Locate and identify every blood parasite.
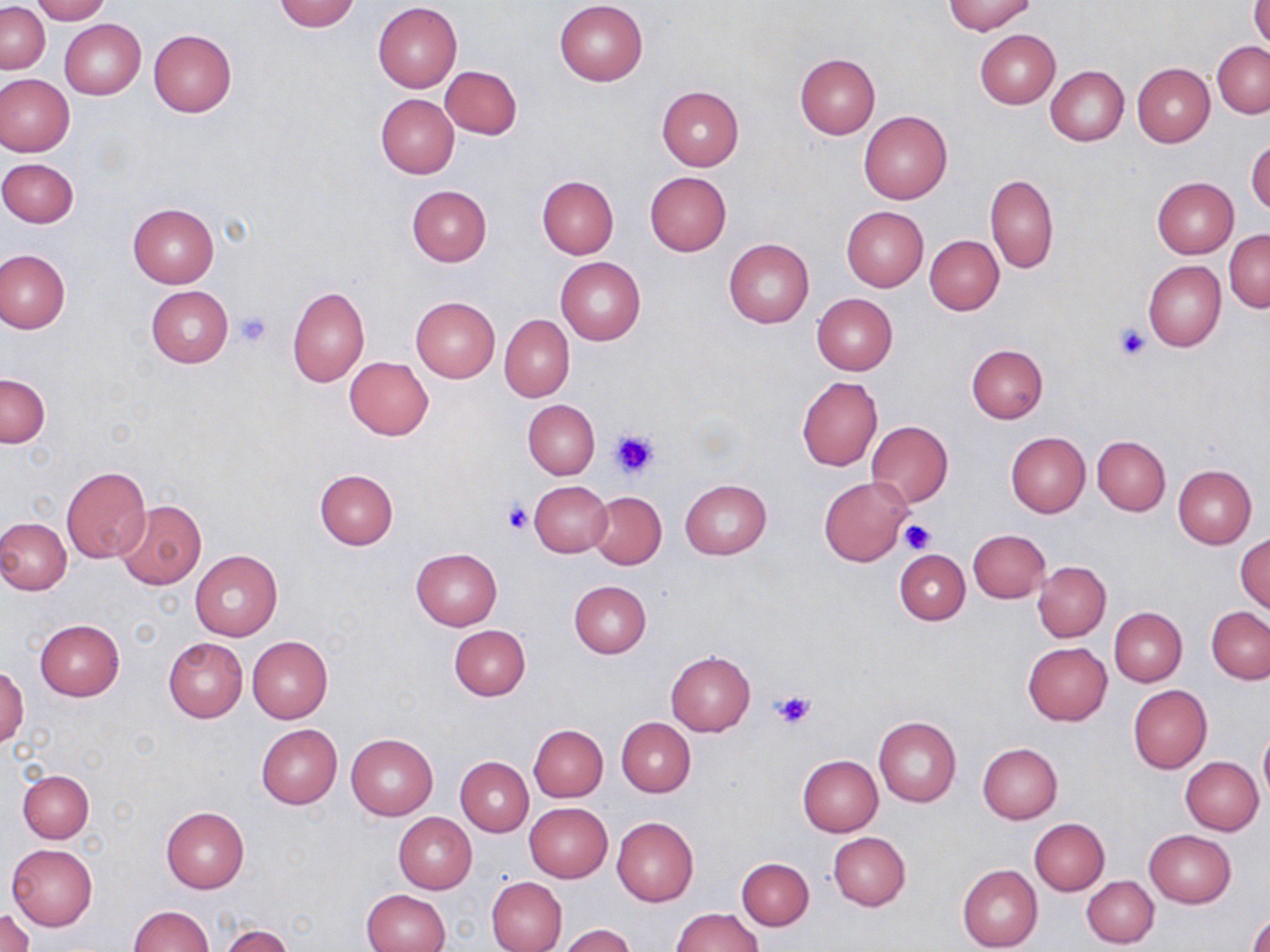

No blood parasites seen.

slide-level diagnosis = no evidence of blood parasites
platelet locations = approximate bounding boxes as named x1/y1/x2/y2 corners in pixels: (x1=231, y1=309, x2=273, y2=346), (x1=1114, y1=324, x2=1150, y2=361), (x1=608, y1=427, x2=662, y2=480), (x1=503, y1=501, x2=534, y2=535), (x1=900, y1=519, x2=936, y2=554), (x1=771, y1=689, x2=816, y2=729)
modality = light microscopy
stain = May-Grünwald-Giemsa
image size = 1270×952 pixels
uninfected red blood cell locations = approximate bounding boxes as named x1/y1/x2/y2 corners in pixels: (x1=30, y1=0, x2=109, y2=23), (x1=274, y1=0, x2=361, y2=32), (x1=943, y1=0, x2=1035, y2=34), (x1=373, y1=1, x2=462, y2=91), (x1=554, y1=1, x2=647, y2=85), (x1=1250, y1=1, x2=1270, y2=51), (x1=1, y1=3, x2=49, y2=73), (x1=59, y1=19, x2=144, y2=99), (x1=975, y1=29, x2=1060, y2=108), (x1=149, y1=30, x2=237, y2=117), (x1=1213, y1=41, x2=1270, y2=117), (x1=794, y1=53, x2=880, y2=138), (x1=1131, y1=63, x2=1214, y2=147), (x1=440, y1=65, x2=521, y2=139), (x1=1045, y1=65, x2=1129, y2=145), (x1=0, y1=75, x2=74, y2=156), (x1=656, y1=86, x2=743, y2=171), (x1=375, y1=93, x2=459, y2=178), (x1=859, y1=110, x2=953, y2=204), (x1=1247, y1=138, x2=1270, y2=214), (x1=0, y1=157, x2=78, y2=227), (x1=644, y1=171, x2=731, y2=256), (x1=985, y1=174, x2=1058, y2=275), (x1=536, y1=176, x2=618, y2=258), (x1=1152, y1=177, x2=1238, y2=258), (x1=406, y1=185, x2=491, y2=267), (x1=127, y1=204, x2=219, y2=288), (x1=841, y1=206, x2=929, y2=291), (x1=1225, y1=230, x2=1269, y2=312), (x1=925, y1=235, x2=1003, y2=315), (x1=723, y1=239, x2=813, y2=328), (x1=0, y1=249, x2=69, y2=332), (x1=555, y1=257, x2=645, y2=344), (x1=1144, y1=260, x2=1226, y2=352), (x1=146, y1=286, x2=233, y2=368), (x1=288, y1=287, x2=369, y2=386), (x1=813, y1=294, x2=897, y2=374), (x1=411, y1=296, x2=500, y2=381), (x1=499, y1=314, x2=574, y2=402), (x1=966, y1=344, x2=1048, y2=423), (x1=344, y1=357, x2=433, y2=440), (x1=1, y1=373, x2=50, y2=447), (x1=796, y1=376, x2=882, y2=471), (x1=523, y1=400, x2=600, y2=479), (x1=866, y1=420, x2=952, y2=508), (x1=1005, y1=431, x2=1090, y2=517), (x1=1093, y1=436, x2=1171, y2=515), (x1=61, y1=465, x2=151, y2=563), (x1=1173, y1=465, x2=1256, y2=548), (x1=314, y1=468, x2=398, y2=550), (x1=819, y1=476, x2=911, y2=565), (x1=680, y1=479, x2=771, y2=559), (x1=529, y1=481, x2=612, y2=558), (x1=589, y1=491, x2=667, y2=568), (x1=116, y1=500, x2=206, y2=590), (x1=0, y1=518, x2=71, y2=596), (x1=968, y1=529, x2=1051, y2=603), (x1=1236, y1=533, x2=1270, y2=614), (x1=411, y1=548, x2=502, y2=631), (x1=894, y1=548, x2=969, y2=624), (x1=190, y1=551, x2=282, y2=640), (x1=1033, y1=561, x2=1111, y2=641), (x1=568, y1=580, x2=651, y2=658), (x1=1109, y1=607, x2=1187, y2=686), (x1=1207, y1=607, x2=1270, y2=683), (x1=34, y1=620, x2=125, y2=701), (x1=448, y1=624, x2=530, y2=700), (x1=247, y1=635, x2=333, y2=722), (x1=163, y1=637, x2=249, y2=722), (x1=1023, y1=642, x2=1112, y2=725), (x1=665, y1=651, x2=755, y2=736), (x1=1, y1=667, x2=28, y2=748), (x1=1129, y1=686, x2=1212, y2=773), (x1=873, y1=716, x2=961, y2=806), (x1=615, y1=717, x2=695, y2=797), (x1=256, y1=723, x2=342, y2=808), (x1=528, y1=725, x2=607, y2=802), (x1=1259, y1=727, x2=1270, y2=804), (x1=346, y1=733, x2=438, y2=820), (x1=976, y1=743, x2=1062, y2=823), (x1=797, y1=754, x2=883, y2=836), (x1=1181, y1=756, x2=1265, y2=835), (x1=456, y1=757, x2=533, y2=835), (x1=18, y1=769, x2=93, y2=842), (x1=525, y1=802, x2=612, y2=882), (x1=161, y1=807, x2=249, y2=893), (x1=392, y1=812, x2=476, y2=893), (x1=612, y1=816, x2=699, y2=905), (x1=1029, y1=818, x2=1110, y2=895), (x1=1144, y1=830, x2=1236, y2=908), (x1=828, y1=831, x2=911, y2=911), (x1=7, y1=842, x2=97, y2=929), (x1=736, y1=857, x2=813, y2=931), (x1=958, y1=864, x2=1043, y2=952), (x1=487, y1=876, x2=568, y2=952), (x1=1083, y1=876, x2=1158, y2=948), (x1=360, y1=889, x2=450, y2=952), (x1=127, y1=906, x2=213, y2=952), (x1=671, y1=908, x2=763, y2=952), (x1=1246, y1=908, x2=1270, y2=952), (x1=2, y1=909, x2=34, y2=952), (x1=220, y1=925, x2=293, y2=952), (x1=558, y1=925, x2=636, y2=952)
magnification = 1000x
field of view = single
preparation = thin blood smear